Assess the morphology of the red blood cells.
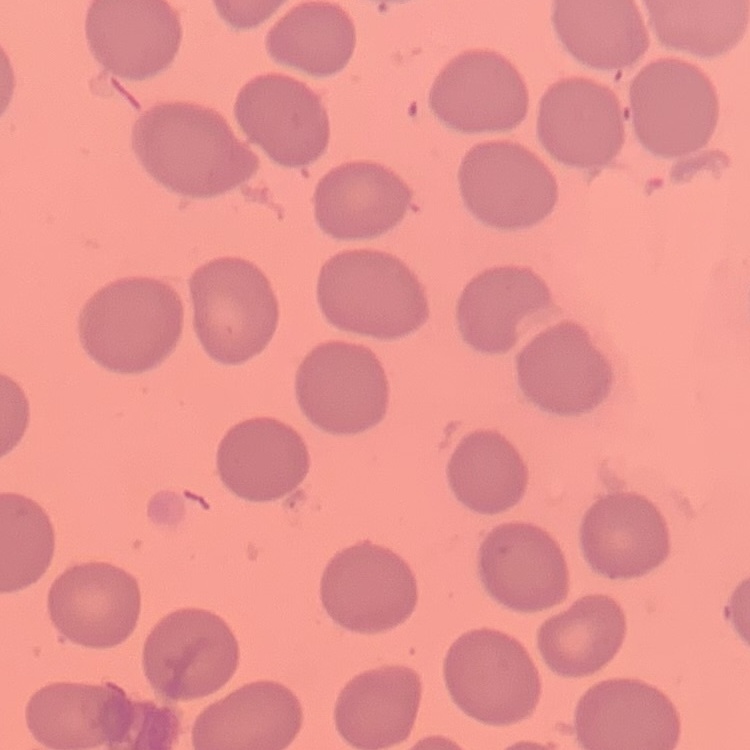
No rouleaux formation.

Thin blood film. One tile cut from a larger photomicrograph. Field's or Giemsa stain.